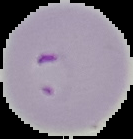
Image is 133×139 pixels. Segmented cell region on a black background. Result: Plasmodium parasites identified. From a thin blood film.